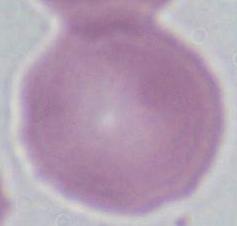
{
  "identification": "red blood cell",
  "magnification": "1000x",
  "modality": "photomicrograph"
}